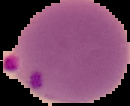
malaria_status: parasitized
preparation: thin blood film
image_type: segmented cell region with the area outside set to black
image_size: 130×106 pixels